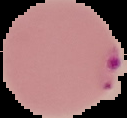

Malaria status: parasitized. Cell region segmented out of the field of view; the surrounding area is masked to black. From a thin blood smear. Image is 127×118 pixels.